Outline each blood parasite and name the species.
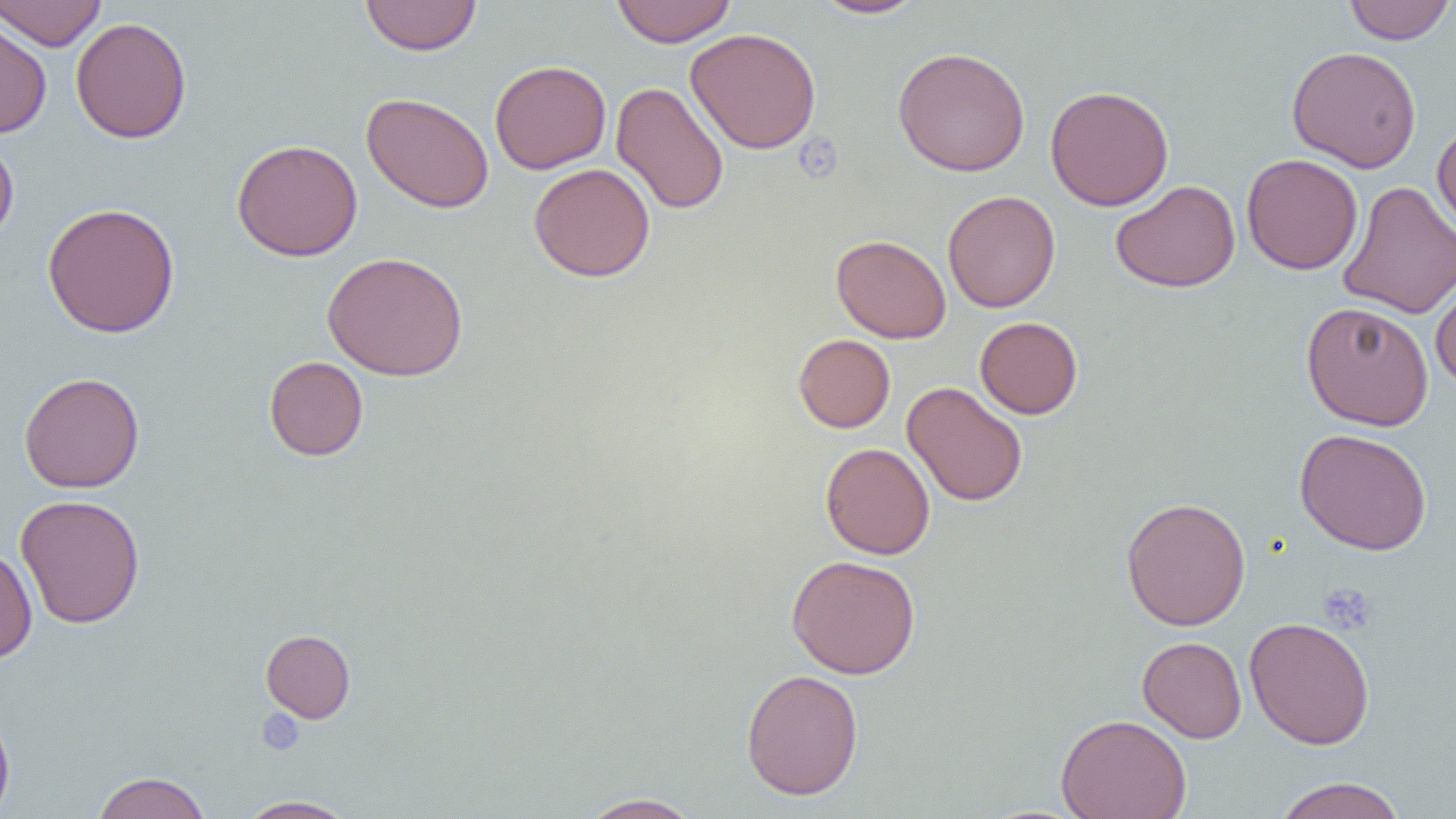

No blood parasites seen.

Approximate bounding boxes as named x1/y1/x2/y2 corners in pixels. Platelet locations: (x1=795, y1=136, x2=842, y2=182), (x1=1318, y1=582, x2=1377, y2=635), (x1=257, y1=709, x2=305, y2=755). Uninfected red blood cell locations: (x1=0, y1=0, x2=107, y2=50), (x1=360, y1=0, x2=482, y2=56), (x1=611, y1=0, x2=736, y2=47), (x1=808, y1=0, x2=927, y2=19), (x1=1342, y1=0, x2=1454, y2=45), (x1=0, y1=14, x2=52, y2=138), (x1=70, y1=17, x2=192, y2=144), (x1=685, y1=27, x2=822, y2=154), (x1=892, y1=46, x2=1030, y2=177), (x1=1286, y1=46, x2=1422, y2=172), (x1=489, y1=60, x2=610, y2=174), (x1=611, y1=81, x2=729, y2=215), (x1=1045, y1=84, x2=1174, y2=211), (x1=361, y1=92, x2=494, y2=213), (x1=1431, y1=121, x2=1456, y2=237), (x1=0, y1=137, x2=19, y2=246), (x1=231, y1=139, x2=363, y2=261), (x1=1241, y1=153, x2=1363, y2=275), (x1=529, y1=163, x2=655, y2=282), (x1=1110, y1=179, x2=1241, y2=293), (x1=1338, y1=181, x2=1455, y2=320), (x1=942, y1=190, x2=1060, y2=313), (x1=42, y1=202, x2=181, y2=338), (x1=831, y1=234, x2=951, y2=344), (x1=322, y1=251, x2=468, y2=381), (x1=1430, y1=272, x2=1456, y2=391), (x1=1301, y1=301, x2=1434, y2=431), (x1=974, y1=316, x2=1084, y2=419), (x1=793, y1=334, x2=895, y2=433), (x1=264, y1=356, x2=368, y2=461), (x1=19, y1=371, x2=145, y2=493), (x1=902, y1=381, x2=1028, y2=507), (x1=1294, y1=428, x2=1432, y2=555), (x1=820, y1=442, x2=935, y2=559), (x1=15, y1=494, x2=145, y2=629), (x1=1120, y1=497, x2=1251, y2=631), (x1=0, y1=546, x2=37, y2=663), (x1=786, y1=554, x2=921, y2=679), (x1=1245, y1=616, x2=1375, y2=750), (x1=261, y1=629, x2=356, y2=722), (x1=1137, y1=636, x2=1247, y2=743), (x1=741, y1=668, x2=864, y2=800), (x1=0, y1=704, x2=15, y2=819), (x1=1056, y1=713, x2=1192, y2=819), (x1=91, y1=771, x2=211, y2=819), (x1=1271, y1=776, x2=1408, y2=819), (x1=579, y1=792, x2=703, y2=819), (x1=236, y1=795, x2=357, y2=818). Slide-level diagnosis: no evidence of blood parasites. Light microscopy. One field of a larger specimen. Image is 1456×819 pixels. 1000x magnification. Thin blood film.